Name the parasite shown.
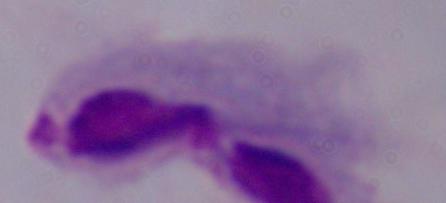
A trichomonad.

Summary:
  - Modality: photomicrograph
  - Magnification: 1000x